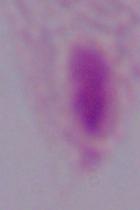

magnification = 1000x
identification = trichomonad
modality = photomicrograph